Report the malaria status of this cell.
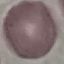

It is uninfected.

Summary:
  - Stain: Giemsa
  - Image type: cell patch, automatically extracted from a larger field of view and resized to 64 × 64 pixels
  - Capture: smartphone through the microscope eyepiece
  - Preparation: thin blood smear